State the blood parasite species.
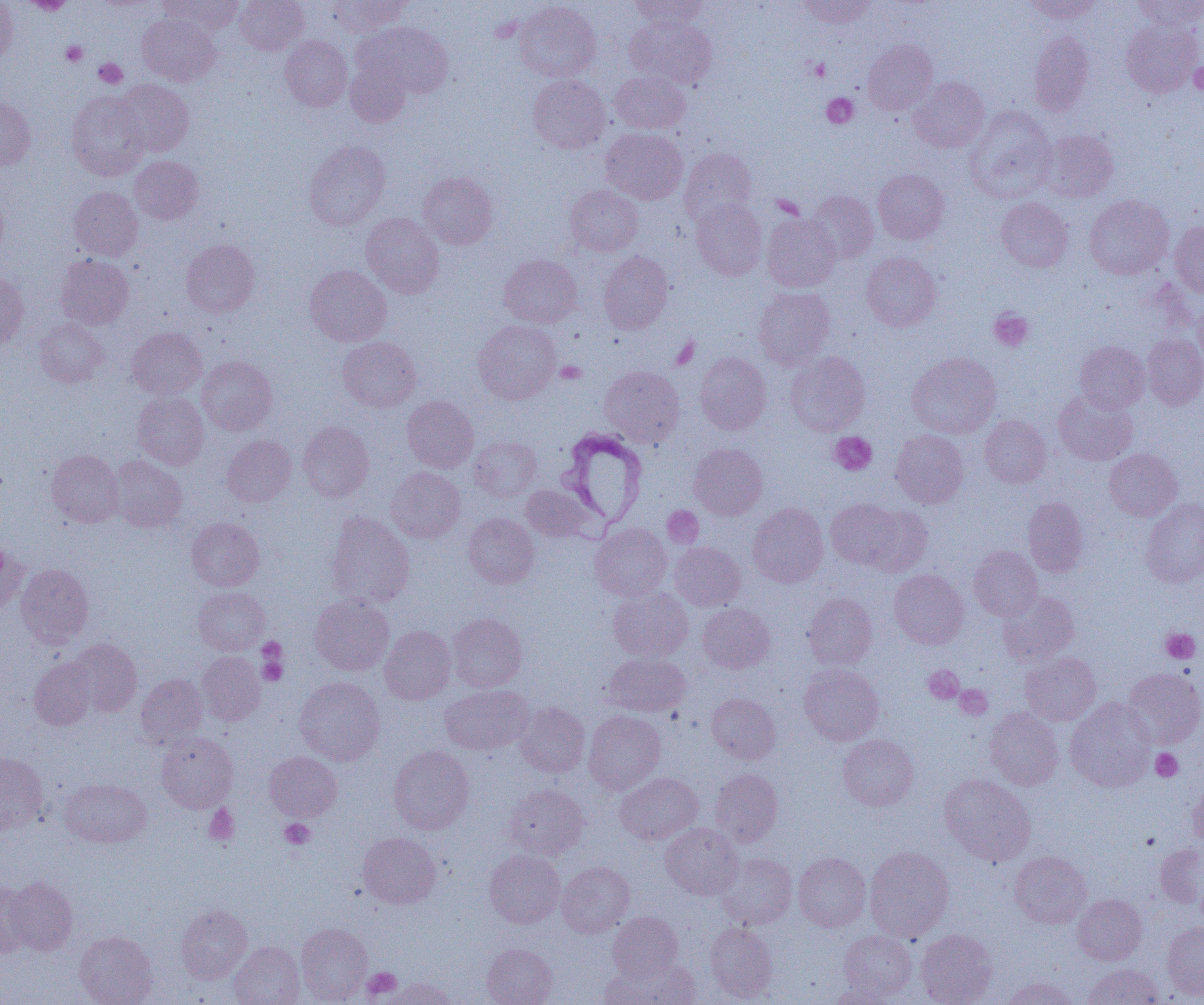
Trypanosoma brucei.

Approximate bounding boxes as (x1,y1)-(x2,y2) corner pairs in pixels. Platelet locations (subset): (62,42)-(87,65), (94,58)-(127,88), (808,58)-(829,80), (1189,60)-(1204,96), (823,93)-(858,128), (989,309)-(1032,351), (556,361)-(586,383), (829,432)-(877,475), (1161,628)-(1200,663), (258,638)-(287,665), (258,655)-(288,685), (924,665)-(964,703), (955,685)-(991,719), (1151,749)-(1182,781), (204,806)-(239,845), (280,818)-(315,850), (363,967)-(402,999). Uninfected red blood cell locations (subset): (0,0)-(17,65), (159,0)-(243,36), (235,0)-(308,55), (328,0)-(410,36), (630,0)-(707,31), (798,0)-(875,29), (1024,0)-(1102,23), (1133,0)-(1204,30), (23,1)-(76,14), (514,1)-(600,82), (137,13)-(220,86), (624,17)-(717,88), (1121,20)-(1202,97), (358,22)-(454,98), (1029,30)-(1093,116), (280,36)-(352,111), (863,40)-(937,115), (345,58)-(412,127), (610,71)-(690,133), (528,74)-(610,153), (909,77)-(989,152), (115,79)-(193,156), (67,91)-(150,181), (0,98)-(35,169), (965,107)-(1057,201), (601,128)-(687,204), (1040,129)-(1118,202), (304,141)-(389,229), (679,148)-(756,225), (129,155)-(203,224), (873,169)-(949,244), (418,172)-(498,249), (565,184)-(643,256), (69,186)-(143,260), (0,188)-(9,263), (808,191)-(878,262), (1085,194)-(1173,279), (996,197)-(1073,272), (690,199)-(767,280), (362,213)-(444,298), (762,213)-(841,292), (1170,221)-(1204,297), (181,239)-(259,317), (598,251)-(673,333), (861,252)-(941,331), (56,254)-(134,329), (499,254)-(582,327), (305,265)-(392,346), (0,272)-(28,350), (754,287)-(834,369), (1193,301)-(1204,370), (35,318)-(108,387), (473,320)-(560,404), (126,327)-(207,399), (1143,335)-(1204,409), (337,336)-(421,411), (1075,340)-(1149,413), (786,351)-(870,435), (695,352)-(771,434), (907,352)-(1001,438), (197,356)-(277,435), (600,366)-(684,446), (1054,391)-(1137,465), (132,392)-(209,469), (402,396)-(479,472), (980,415)-(1050,487), (298,421)-(374,502), (891,429)-(968,508), (222,435)-(296,506), (469,437)-(542,501), (689,443)-(768,519), (1104,448)-(1182,520), (46,449)-(123,527), (108,456)-(186,532), (386,467)-(465,543), (521,485)-(592,542), (1023,497)-(1088,576), (1141,498)-(1204,587), (826,499)-(904,570), (747,503)-(828,587), (861,505)-(932,577), (325,512)-(415,608), (463,513)-(539,588), (187,517)-(264,591), (590,523)-(672,601), (670,542)-(745,610), (0,544)-(29,616), (969,546)-(1042,620), (16,564)-(93,647), (889,569)-(968,648), (194,587)-(270,655), (608,588)-(693,661), (999,591)-(1079,666), (803,593)-(877,669), (310,595)-(394,675), (697,603)-(774,673), (448,613)-(527,692), (380,626)-(455,704), (68,638)-(142,716), (198,651)-(265,725), (1021,652)-(1100,725), (605,653)-(690,716), (29,657)-(97,730), (800,663)-(883,744), (1123,667)-(1204,748), (136,674)-(207,748), (294,677)-(384,765), (440,685)-(534,754), (707,693)-(781,763), (1066,698)-(1157,791), (515,702)-(589,777), (985,708)-(1064,789), (584,710)-(666,794), (156,731)-(238,813), (838,734)-(919,810), (389,745)-(474,834), (265,751)-(341,821), (0,752)-(48,835), (711,768)-(782,846), (615,772)-(702,844), (939,774)-(1035,865), (60,778)-(151,847), (1188,781)-(1204,849), (504,784)-(588,860), (661,823)-(743,899), (358,832)-(441,908), (1155,844)-(1204,909), (865,846)-(954,940), (485,849)-(565,927), (1010,851)-(1091,928), (717,853)-(797,929), (793,853)-(871,931), (557,861)-(634,937), (4,876)-(77,955), (0,880)-(34,957), (1073,894)-(1147,965), (175,904)-(252,984), (607,911)-(682,980), (706,922)-(778,1002), (1163,922)-(1204,1000), (296,923)-(372,1004), (916,929)-(997,1005), (839,930)-(917,1000), (75,931)-(158,1005), (229,941)-(304,1005), (482,943)-(557,1005), (610,957)-(700,1005), (1083,964)-(1162,1005), (386,977)-(458,1005), (1001,978)-(1079,1005), (827,982)-(900,1005). Trypanosoma brucei locations: (560,429)-(648,530). Thin blood smear. Single field of view. Optical microscopy. Image is 1204×1005 pixels. 1000x magnification.